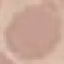

Malaria status: uninfected. Acquired by smartphone through the microscope eyepiece. Giemsa stain. Thin smear of blood. Cell patch, automatically extracted from a larger field of view and resized to 64 × 64 pixels.